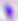

Summary:
  - Identification: Toxoplasma gondii
  - Magnification: 400x
  - Modality: photomicrograph